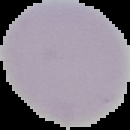

Summary:
  - Image type: segmented cell region with the area outside set to black
  - Malaria status: uninfected
  - Preparation: thin blood film
  - Image size: 130×130 pixels